Evaluate for malaria.
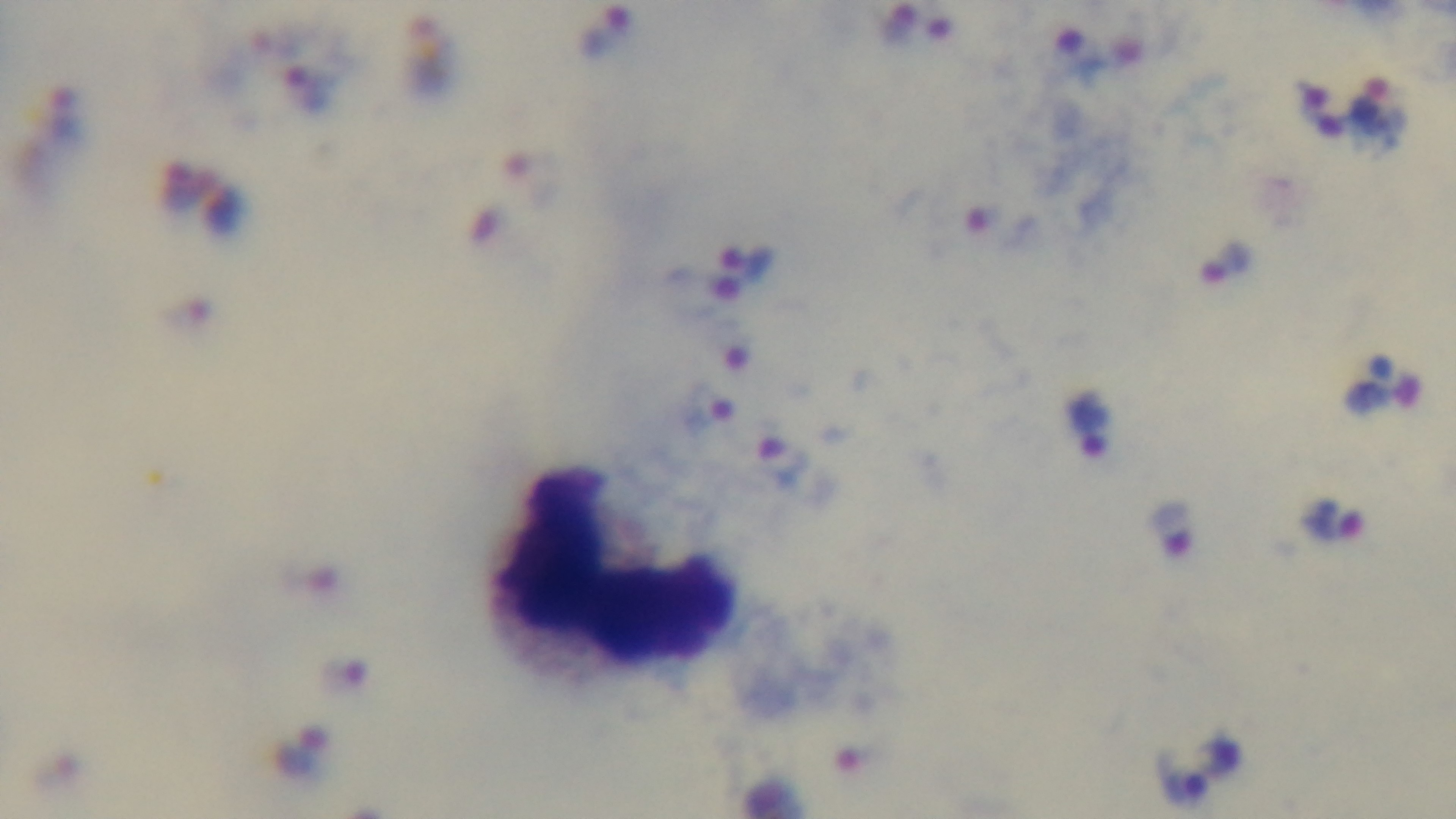

Infected.

stain = Giemsa
preparation = thick blood film
objective = 100x oil immersion
field of view = one from the slide
modality = light microscopy
capture = mounted 4K digital camera